Identify the parasite.
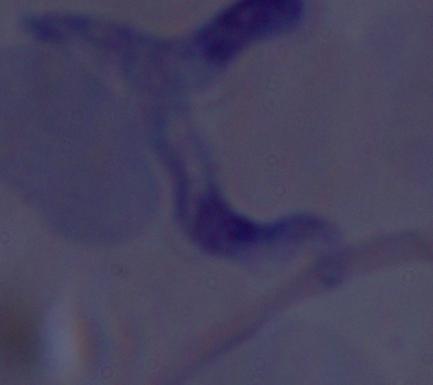
This is a trypanosome.

Summary:
  - Modality: micrograph
  - Magnification: 1000x